Locate every blood parasite and identify its species.
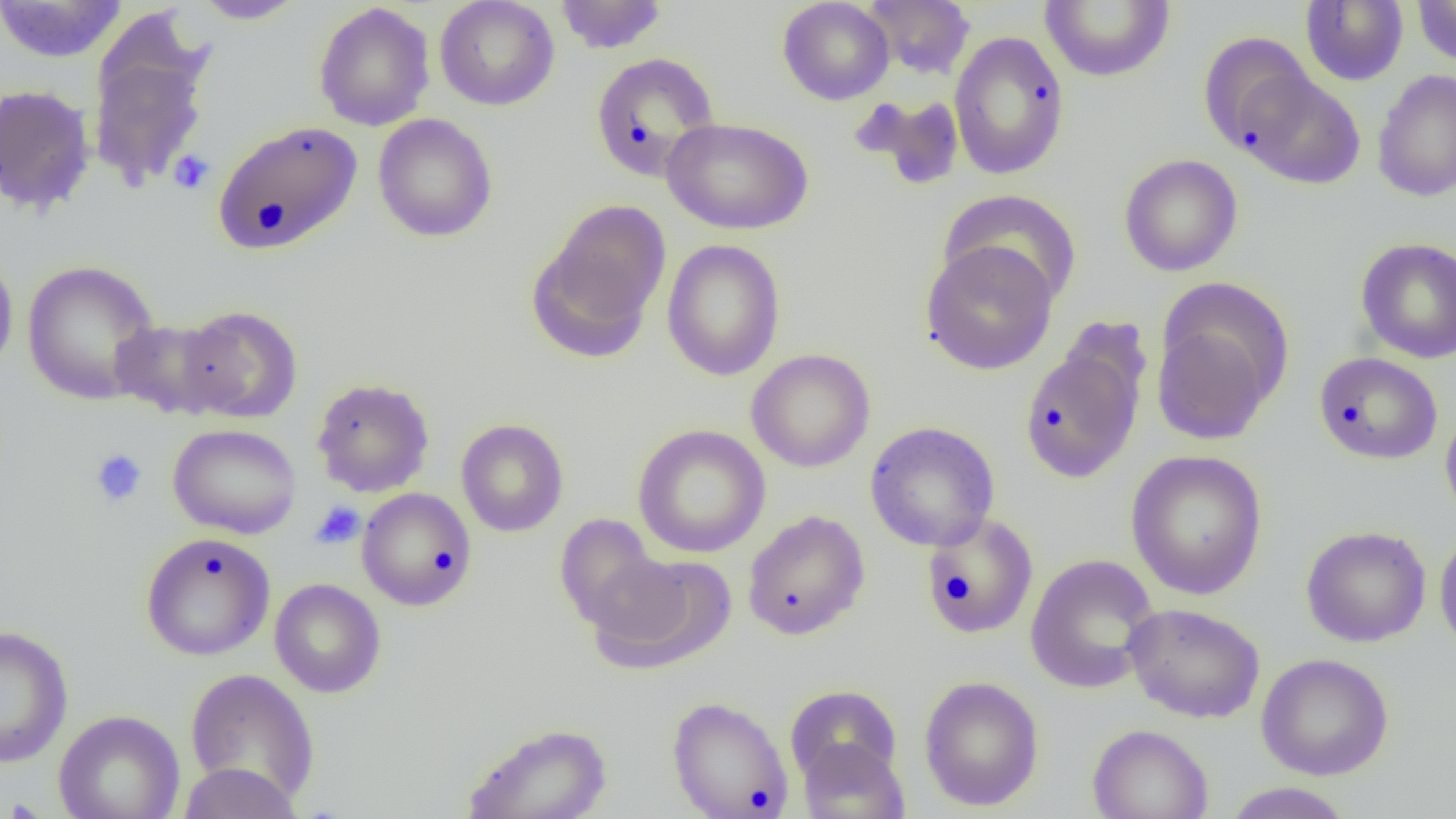

No blood parasites seen.

Summary:
  - Coordinate format: approximate bounding boxes as (x1, y1, x2, y2) in pixels
  - Uninfected red blood cell locations: (0, 0, 129, 63), (190, 0, 306, 24), (434, 0, 560, 111), (554, 0, 667, 54), (777, 0, 894, 105), (862, 0, 976, 80), (1039, 0, 1176, 83), (1300, 0, 1409, 86), (1412, 1, 1456, 66), (313, 2, 435, 132), (86, 25, 214, 195), (949, 30, 1070, 180), (1198, 33, 1319, 157), (590, 52, 721, 182), (1372, 68, 1456, 202), (1240, 70, 1365, 189), (0, 84, 96, 216), (852, 93, 967, 191), (373, 113, 498, 242), (661, 117, 814, 235), (212, 120, 363, 255), (1118, 153, 1243, 277), (939, 189, 1083, 309), (529, 199, 672, 358), (1355, 237, 1456, 363), (661, 239, 786, 381), (919, 241, 1058, 375), (0, 246, 19, 381), (21, 260, 161, 406), (175, 305, 303, 423), (1151, 308, 1281, 446), (109, 317, 235, 420), (1019, 343, 1146, 483), (746, 348, 875, 473), (1313, 352, 1443, 465), (311, 377, 435, 498), (1440, 403, 1456, 524), (456, 418, 569, 537), (865, 421, 1000, 552), (168, 423, 302, 539), (632, 424, 771, 558), (1126, 450, 1268, 600), (357, 487, 477, 610), (742, 510, 870, 640), (922, 513, 1040, 639), (554, 514, 664, 634), (1301, 525, 1431, 647), (1434, 527, 1456, 656), (140, 532, 276, 661), (587, 553, 736, 674), (1024, 554, 1160, 695), (269, 578, 386, 698), (1123, 602, 1265, 723), (0, 625, 73, 768), (1256, 653, 1394, 780), (184, 669, 320, 804), (919, 675, 1044, 811), (785, 685, 902, 786), (667, 696, 793, 818), (53, 709, 185, 819), (462, 722, 613, 819), (1086, 724, 1214, 819), (796, 737, 909, 819), (177, 761, 304, 818), (1222, 782, 1356, 819)
  - Platelet locations: (168, 149, 215, 195), (89, 448, 148, 508), (310, 500, 366, 550)
  - Slide-level diagnosis: no evidence of blood parasites
  - Image size: 1456×819 pixels
  - Modality: optical microscopy
  - Magnification: 1000x
  - Preparation: thin blood film
  - Field of view: one of a larger specimen